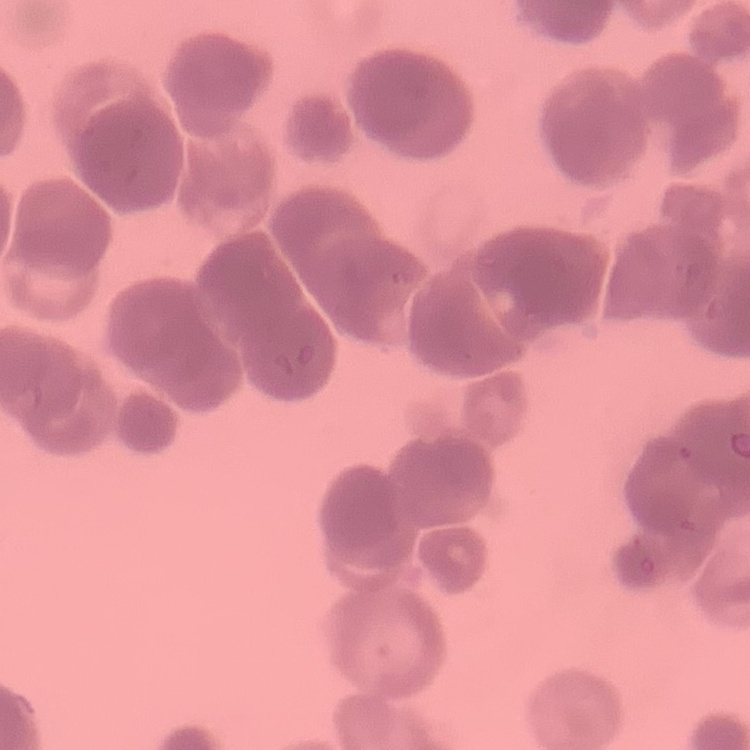
Summary:
  - Red blood cell morphology: rouleaux formation
  - Image type: one tile cut from a larger photomicrograph
  - Stain: Field's or Giemsa
  - Preparation: thin blood film